Locate and identify every blood parasite.
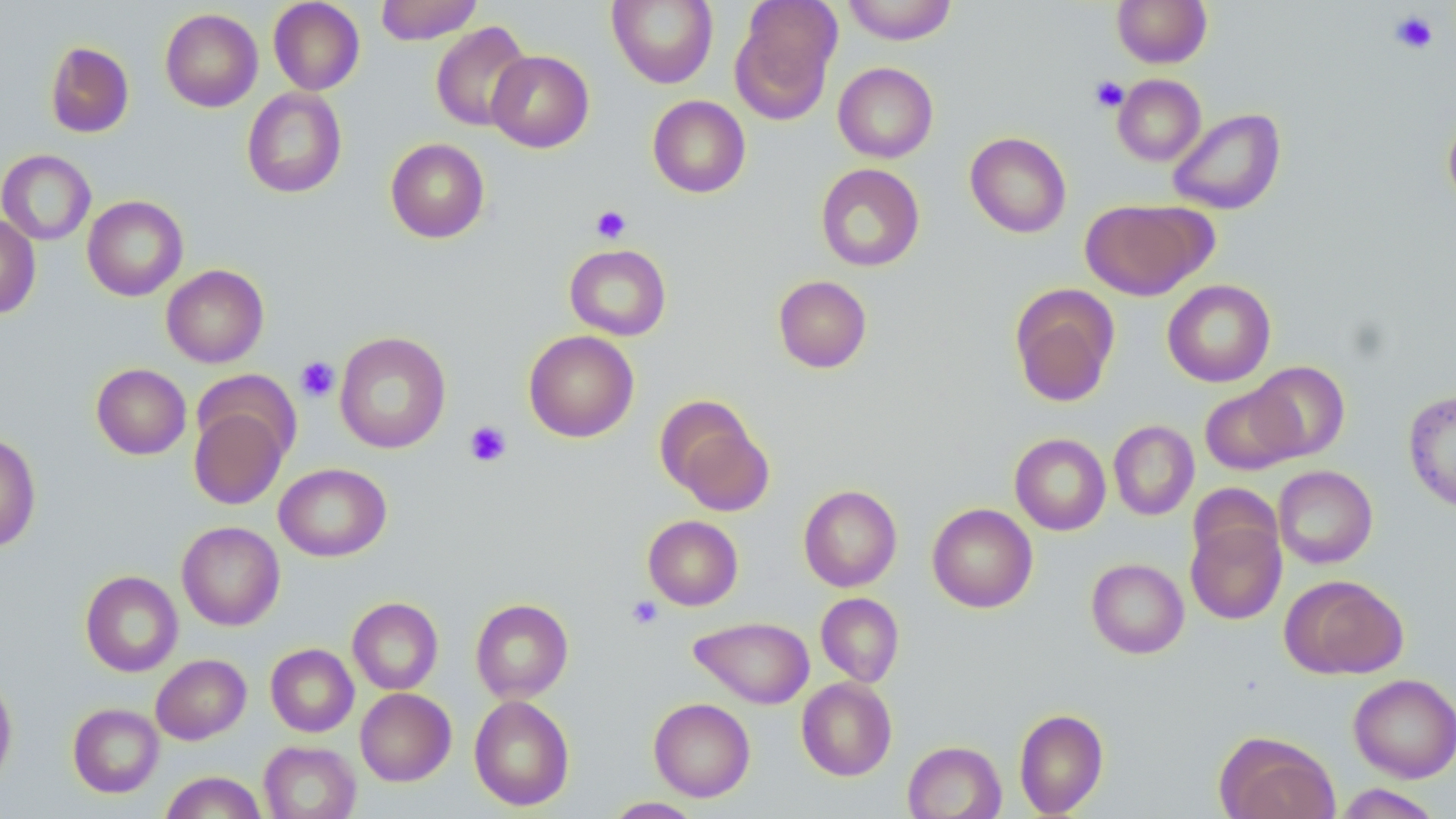

No blood parasites observed.

slide-level diagnosis = no evidence of blood parasites
magnification = 1000x
stain = May-Grünwald-Giemsa
image size = 1456×819 pixels
platelet locations = approximate bounding boxes as named x1/y1/x2/y2 corners in pixels: (x1=1390, y1=10, x2=1438, y2=54), (x1=1090, y1=76, x2=1129, y2=113), (x1=591, y1=205, x2=631, y2=244), (x1=295, y1=356, x2=340, y2=402), (x1=464, y1=420, x2=512, y2=468), (x1=626, y1=595, x2=663, y2=630)
uninfected red blood cell locations = approximate bounding boxes as named x1/y1/x2/y2 corners in pixels: (x1=375, y1=0, x2=483, y2=45), (x1=607, y1=0, x2=718, y2=88), (x1=842, y1=0, x2=957, y2=45), (x1=1111, y1=0, x2=1212, y2=68), (x1=268, y1=1, x2=365, y2=95), (x1=731, y1=2, x2=842, y2=123), (x1=160, y1=8, x2=263, y2=112), (x1=430, y1=21, x2=533, y2=132), (x1=45, y1=41, x2=134, y2=138), (x1=486, y1=50, x2=594, y2=152), (x1=833, y1=62, x2=938, y2=163), (x1=1112, y1=74, x2=1206, y2=166), (x1=242, y1=87, x2=347, y2=198), (x1=648, y1=95, x2=751, y2=198), (x1=1167, y1=107, x2=1286, y2=215), (x1=1443, y1=111, x2=1456, y2=211), (x1=965, y1=132, x2=1071, y2=238), (x1=385, y1=138, x2=489, y2=243), (x1=0, y1=150, x2=96, y2=245), (x1=815, y1=163, x2=925, y2=271), (x1=82, y1=195, x2=188, y2=301), (x1=1081, y1=199, x2=1209, y2=300), (x1=0, y1=214, x2=40, y2=319), (x1=564, y1=244, x2=672, y2=340), (x1=161, y1=264, x2=269, y2=367), (x1=773, y1=275, x2=872, y2=373), (x1=1162, y1=279, x2=1275, y2=387), (x1=1010, y1=285, x2=1119, y2=407), (x1=523, y1=330, x2=639, y2=442), (x1=334, y1=331, x2=451, y2=454), (x1=1248, y1=361, x2=1350, y2=461), (x1=91, y1=363, x2=191, y2=459), (x1=1200, y1=384, x2=1301, y2=475), (x1=1403, y1=389, x2=1456, y2=512), (x1=659, y1=400, x2=774, y2=513), (x1=189, y1=403, x2=290, y2=510), (x1=1108, y1=420, x2=1199, y2=520), (x1=0, y1=433, x2=41, y2=551), (x1=1010, y1=433, x2=1111, y2=535), (x1=274, y1=463, x2=391, y2=561), (x1=1273, y1=465, x2=1378, y2=568), (x1=1187, y1=483, x2=1282, y2=569), (x1=798, y1=484, x2=902, y2=592), (x1=926, y1=503, x2=1038, y2=613), (x1=643, y1=515, x2=743, y2=610), (x1=1186, y1=517, x2=1287, y2=624), (x1=177, y1=521, x2=285, y2=631), (x1=1086, y1=558, x2=1189, y2=658), (x1=80, y1=570, x2=183, y2=676), (x1=1280, y1=574, x2=1408, y2=679), (x1=816, y1=592, x2=904, y2=686), (x1=347, y1=597, x2=443, y2=694), (x1=470, y1=598, x2=573, y2=703), (x1=690, y1=616, x2=814, y2=708), (x1=266, y1=643, x2=359, y2=737), (x1=151, y1=653, x2=251, y2=745), (x1=0, y1=673, x2=18, y2=788), (x1=1348, y1=673, x2=1456, y2=783), (x1=796, y1=677, x2=897, y2=781), (x1=355, y1=688, x2=456, y2=786), (x1=468, y1=695, x2=575, y2=811), (x1=649, y1=698, x2=755, y2=801), (x1=68, y1=703, x2=164, y2=798), (x1=1014, y1=708, x2=1109, y2=817), (x1=1215, y1=731, x2=1339, y2=819), (x1=259, y1=741, x2=360, y2=819), (x1=903, y1=741, x2=1006, y2=819), (x1=160, y1=771, x2=267, y2=818), (x1=1333, y1=784, x2=1443, y2=818), (x1=602, y1=797, x2=705, y2=818)
preparation = thin blood film
field of view = one of a larger specimen
modality = light microscopy